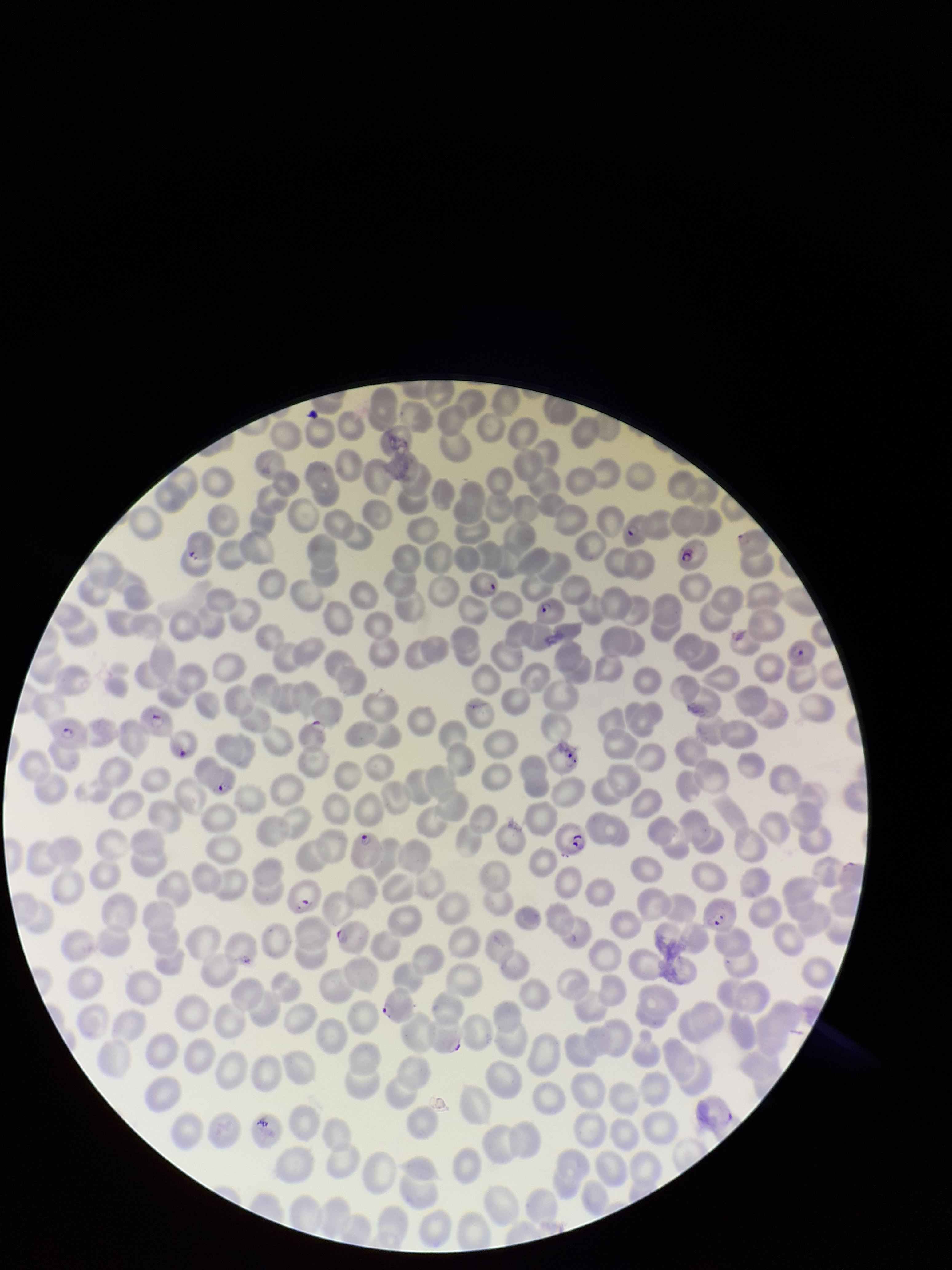

parasitized red blood cell count = 17
preparation = thin smear
parasitized red blood cells = detected
red blood cell count = 252
image size = 952×1270 pixels
species reported for this patient = Plasmodium falciparum
stain = Giemsa
capture = smartphone photograph through the microscope eyepiece
patient malaria status = infected
field of view = one from this slide